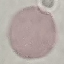

malaria_status: uninfected
image_type: automatically extracted cell patch, resized to 64 × 64 pixels
preparation: thin smear
capture: smartphone camera at the microscope eyepiece
stain: Giemsa